Locate every Plasmodium parasite and identify its life-cycle stage.
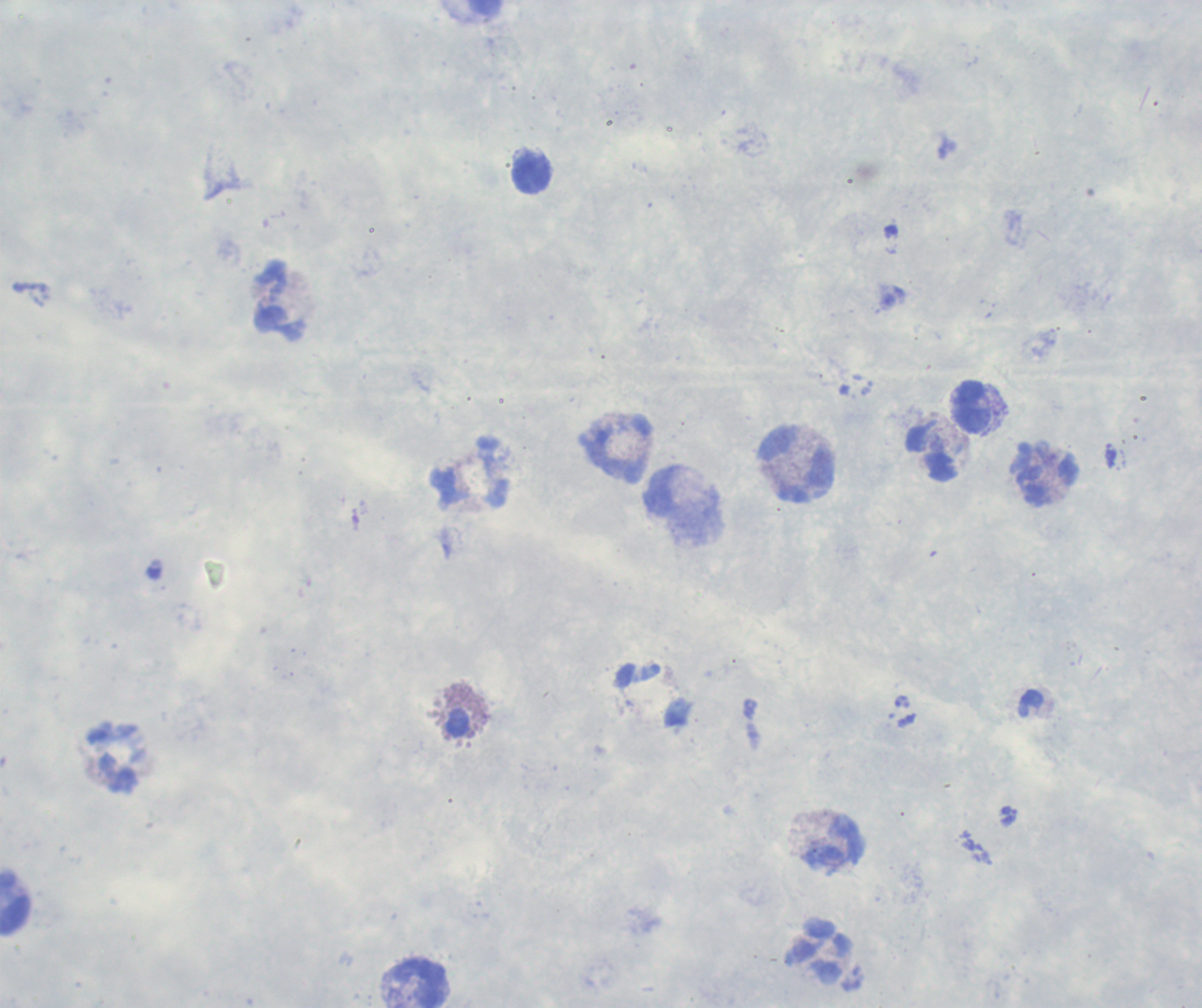
No Plasmodium parasites detected.

Approximate object centers, in pixels from the top-left corner. Leukocyte locations: (x=531, y=173), (x=281, y=301), (x=972, y=407), (x=617, y=450), (x=933, y=454), (x=799, y=466), (x=475, y=474), (x=1047, y=475), (x=117, y=759), (x=835, y=843), (x=15, y=904), (x=823, y=954), (x=423, y=984). Background quality: poor. Image is 1202×1008 pixels. Captured at 100x magnification. Romanowsky-stained preparation. Single field of view. Thick smear of blood. Previously used in a real diagnosis. Coloration quality: good.